Report the malaria status of this cell.
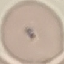
It is uninfected.

Giemsa-stained preparation. Thin smear of blood. Photographed with a smartphone camera at the microscope eyepiece. Automatically extracted cell patch, resized to 64 × 64 pixels.